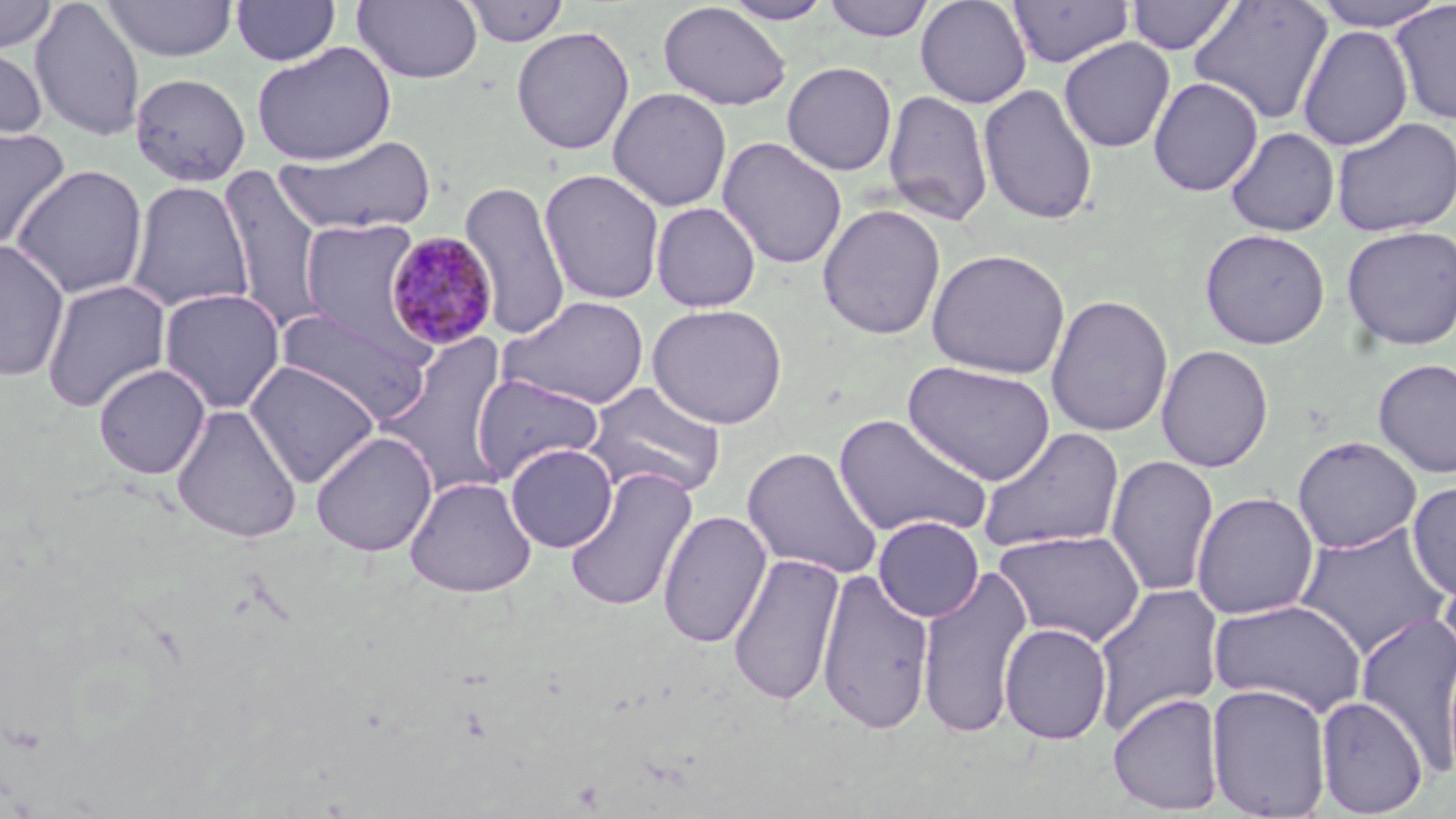
Summary:
  - Coordinate format: approximate bounding boxes as [x1, y1, x2, y2] in pixels
  - Uninfected red blood cell locations: [0, 0, 59, 55], [29, 0, 146, 141], [231, 0, 342, 66], [352, 0, 484, 84], [459, 0, 570, 46], [823, 0, 935, 41], [915, 0, 1032, 108], [1007, 0, 1133, 68], [1126, 0, 1239, 56], [1312, 0, 1448, 31], [102, 1, 239, 61], [722, 1, 834, 24], [1189, 1, 1333, 126], [1389, 1, 1456, 125], [658, 2, 792, 111], [1297, 24, 1413, 151], [511, 26, 635, 155], [1058, 37, 1176, 153], [0, 41, 48, 145], [251, 42, 396, 166], [782, 61, 897, 175], [130, 73, 252, 186], [1148, 77, 1264, 196], [977, 83, 1099, 225], [607, 86, 733, 212], [882, 89, 993, 227], [1330, 116, 1456, 238], [0, 126, 70, 250], [1225, 127, 1340, 236], [275, 134, 437, 236], [717, 137, 848, 270], [10, 164, 148, 300], [217, 165, 328, 332], [539, 168, 665, 305], [459, 179, 570, 341], [126, 180, 253, 314], [651, 202, 761, 312], [818, 204, 946, 340], [299, 218, 425, 350], [1341, 225, 1456, 351], [1199, 228, 1331, 349], [0, 239, 70, 382], [926, 248, 1071, 379], [41, 279, 171, 413], [158, 287, 286, 414], [1045, 293, 1174, 437], [499, 295, 650, 409], [647, 303, 787, 429], [275, 308, 433, 423], [376, 332, 515, 500], [1156, 344, 1274, 473], [1373, 358, 1456, 478], [244, 360, 381, 487], [903, 361, 1055, 485], [93, 363, 211, 479], [471, 373, 604, 484], [584, 381, 727, 500], [171, 404, 303, 543], [833, 413, 993, 540], [976, 427, 1126, 555], [310, 430, 437, 557], [1292, 435, 1422, 554], [504, 443, 618, 552], [742, 446, 883, 580], [1105, 454, 1220, 597], [564, 466, 698, 613], [405, 476, 537, 597], [1407, 481, 1456, 600], [1191, 491, 1319, 619], [658, 510, 771, 649], [872, 515, 984, 622], [1294, 523, 1452, 658], [993, 529, 1147, 647], [728, 551, 845, 707], [1437, 561, 1456, 677], [916, 562, 1034, 740], [817, 567, 935, 736], [1090, 582, 1225, 737], [1207, 598, 1368, 718], [1355, 609, 1456, 775], [1000, 622, 1112, 744], [1206, 683, 1332, 819], [1107, 692, 1225, 815], [1315, 695, 1428, 817]
  - Plasmodium malariae-infected red blood cell locations: [384, 233, 499, 353]
  - Slide-level diagnosis: Plasmodium malariae
  - Modality: light microscopy
  - Preparation: thin blood smear
  - Magnification: 1000x
  - Image size: 1456×819 pixels
  - Field of view: one of a larger specimen
  - Stain: May-Grünwald-Giemsa